Comment on the morphology of the erythrocytes.
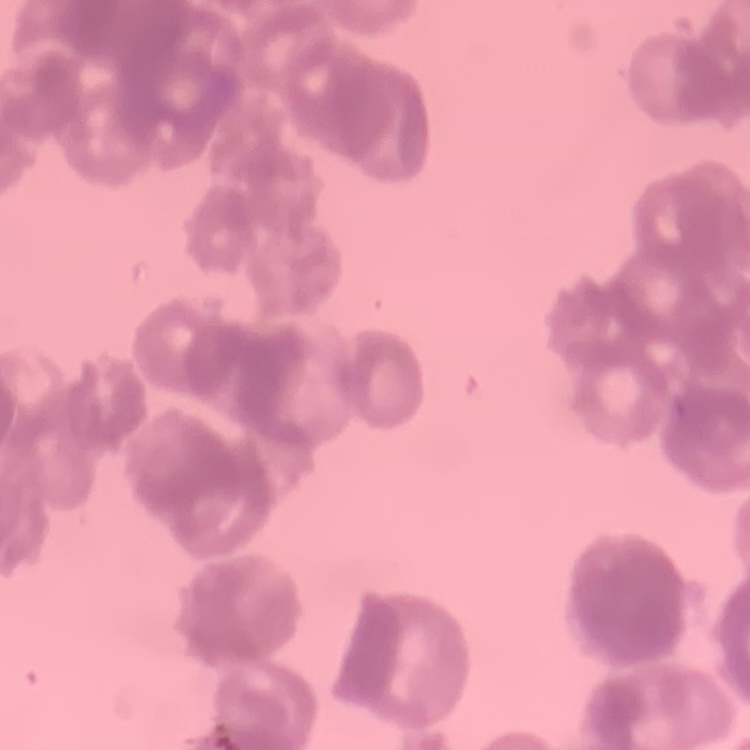
They show rouleaux formation.

preparation = thin blood smear
image type = square crop of a larger photomicrograph
stain = Field's or Giemsa